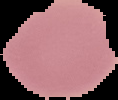

image_type: segmented cell region on a black background
result: no malaria parasites seen
preparation: thin blood smear
image_size: 118×100 pixels